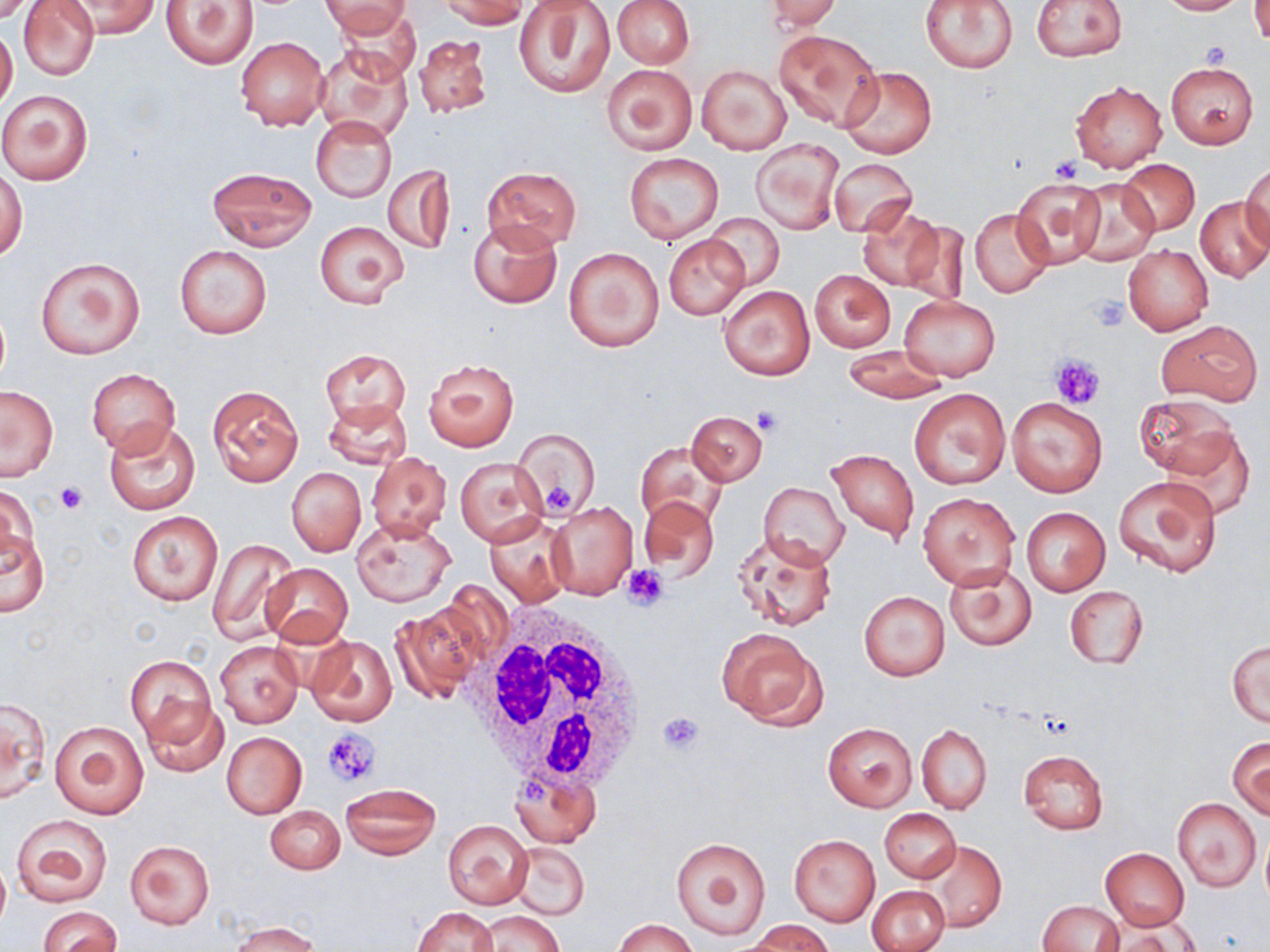 Approximate bounding boxes as [x1, y1, x2, y2] in pixels. Uninfected red blood cell locations: [18, 0, 100, 81], [62, 0, 161, 38], [162, 0, 259, 69], [322, 0, 416, 44], [612, 0, 694, 68], [759, 0, 841, 32], [921, 0, 1019, 74], [1031, 0, 1128, 62], [1157, 0, 1247, 15], [1249, 0, 1269, 46], [437, 1, 530, 29], [513, 3, 615, 99], [0, 25, 17, 112], [774, 29, 884, 130], [413, 32, 495, 119], [235, 37, 328, 131], [313, 45, 413, 142], [1164, 60, 1259, 148], [603, 64, 697, 155], [697, 65, 791, 155], [839, 66, 936, 159], [1070, 81, 1168, 173], [0, 87, 97, 186], [310, 115, 395, 202], [752, 139, 843, 235], [623, 152, 724, 245], [829, 158, 917, 238], [1117, 159, 1200, 235], [1242, 162, 1270, 253], [383, 164, 455, 255], [481, 166, 582, 250], [208, 167, 316, 250], [0, 168, 28, 262], [1010, 177, 1110, 271], [1067, 178, 1161, 266], [1196, 196, 1270, 283], [858, 204, 946, 294], [969, 208, 1054, 298], [704, 214, 785, 290], [468, 219, 563, 310], [314, 220, 409, 308], [663, 235, 750, 320], [1123, 243, 1213, 336], [175, 244, 272, 339], [562, 247, 664, 351], [35, 256, 144, 360], [809, 270, 896, 352], [718, 285, 814, 380], [899, 296, 999, 381], [1156, 319, 1263, 406], [839, 345, 951, 403], [320, 349, 410, 426], [423, 358, 519, 450], [87, 369, 179, 456], [207, 384, 304, 488], [0, 385, 58, 480], [909, 388, 1010, 489], [1136, 393, 1239, 478], [1006, 397, 1107, 497], [322, 400, 412, 469], [688, 411, 766, 485], [103, 418, 202, 515], [1155, 424, 1257, 518], [515, 426, 602, 519], [638, 441, 728, 530], [826, 448, 919, 543], [367, 451, 452, 542], [454, 456, 548, 546], [287, 467, 366, 557], [1113, 474, 1224, 579], [758, 482, 849, 568], [1, 484, 37, 577], [918, 492, 1019, 589], [639, 495, 721, 581], [546, 500, 638, 601], [1021, 507, 1110, 595], [127, 511, 222, 607], [484, 514, 572, 608], [349, 518, 456, 607], [0, 528, 49, 617], [732, 530, 837, 631], [206, 537, 300, 645], [944, 563, 1037, 651], [261, 564, 351, 647], [1065, 586, 1148, 669], [859, 591, 950, 680], [388, 606, 482, 703], [716, 628, 825, 729], [305, 635, 398, 727], [214, 640, 302, 728], [1228, 640, 1269, 727], [126, 655, 217, 752], [139, 695, 229, 778], [1, 697, 50, 806], [49, 719, 150, 819], [823, 722, 915, 811], [917, 724, 992, 814], [222, 732, 307, 818], [1229, 737, 1269, 819], [1017, 750, 1109, 834], [510, 768, 601, 845], [340, 783, 441, 860], [1172, 798, 1261, 891], [266, 805, 345, 874], [880, 809, 960, 883], [10, 814, 113, 907], [442, 818, 533, 908], [789, 834, 879, 925], [670, 836, 774, 941], [126, 840, 214, 928], [916, 841, 1006, 931], [509, 842, 590, 921], [1101, 848, 1189, 930], [0, 858, 9, 933], [868, 885, 949, 952], [1037, 900, 1123, 951], [38, 906, 121, 952], [411, 906, 499, 952], [474, 911, 562, 952], [1103, 917, 1198, 951], [613, 919, 697, 952], [231, 920, 322, 952], [747, 920, 835, 952]. White blood cell locations: [466, 603, 648, 794]. Platelet locations: [1203, 41, 1233, 66], [1049, 156, 1084, 185], [1090, 293, 1131, 330], [1049, 353, 1105, 408], [751, 409, 783, 436], [54, 481, 88, 513], [544, 485, 575, 512], [623, 562, 670, 610], [658, 710, 704, 756], [322, 728, 380, 789]. Slide-level diagnosis: no evidence of blood parasites. Image is 1270×952 pixels. Captured at 1000x magnification. Optical microscopy. Thin blood film. May-Grünwald-Giemsa-stained preparation. Single field of view.